Name the parasite shown.
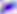

Toxoplasma gondii.

Summary:
  - Modality: photomicrograph
  - Magnification: 400x